Locate Plasmodium parasites and leukocytes.
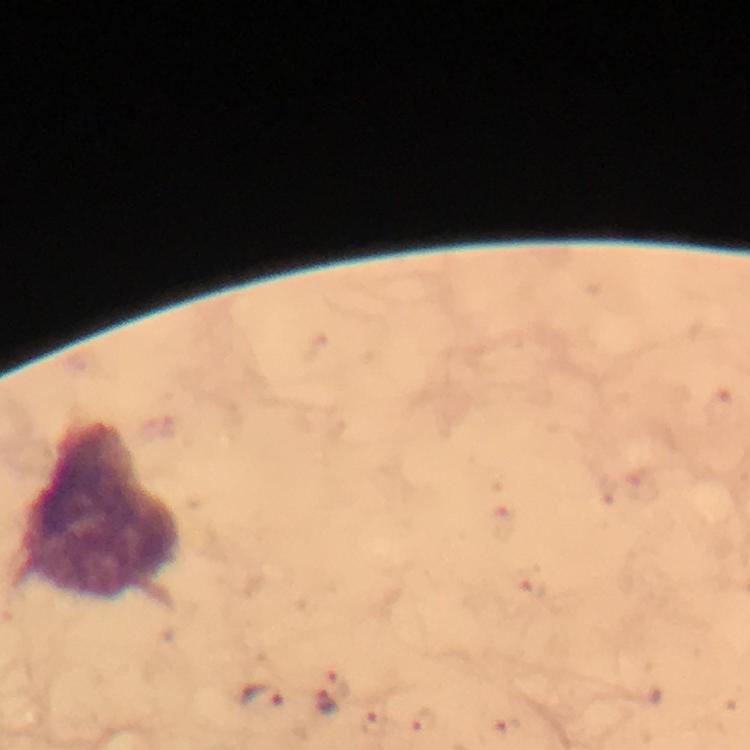

Approximate centers as [x, y] in pixels.
Plasmodium parasites: [340, 684], [262, 698], [326, 704].
Leukocytes: [101, 513].

Image is 750×750 pixels. Thick blood smear. Immersion oil was used. Cropped region of a single field of view. At 100x magnification. Photographed through the microscope with a smartphone camera. Giemsa stain. From a diagnostic examination for malaria.